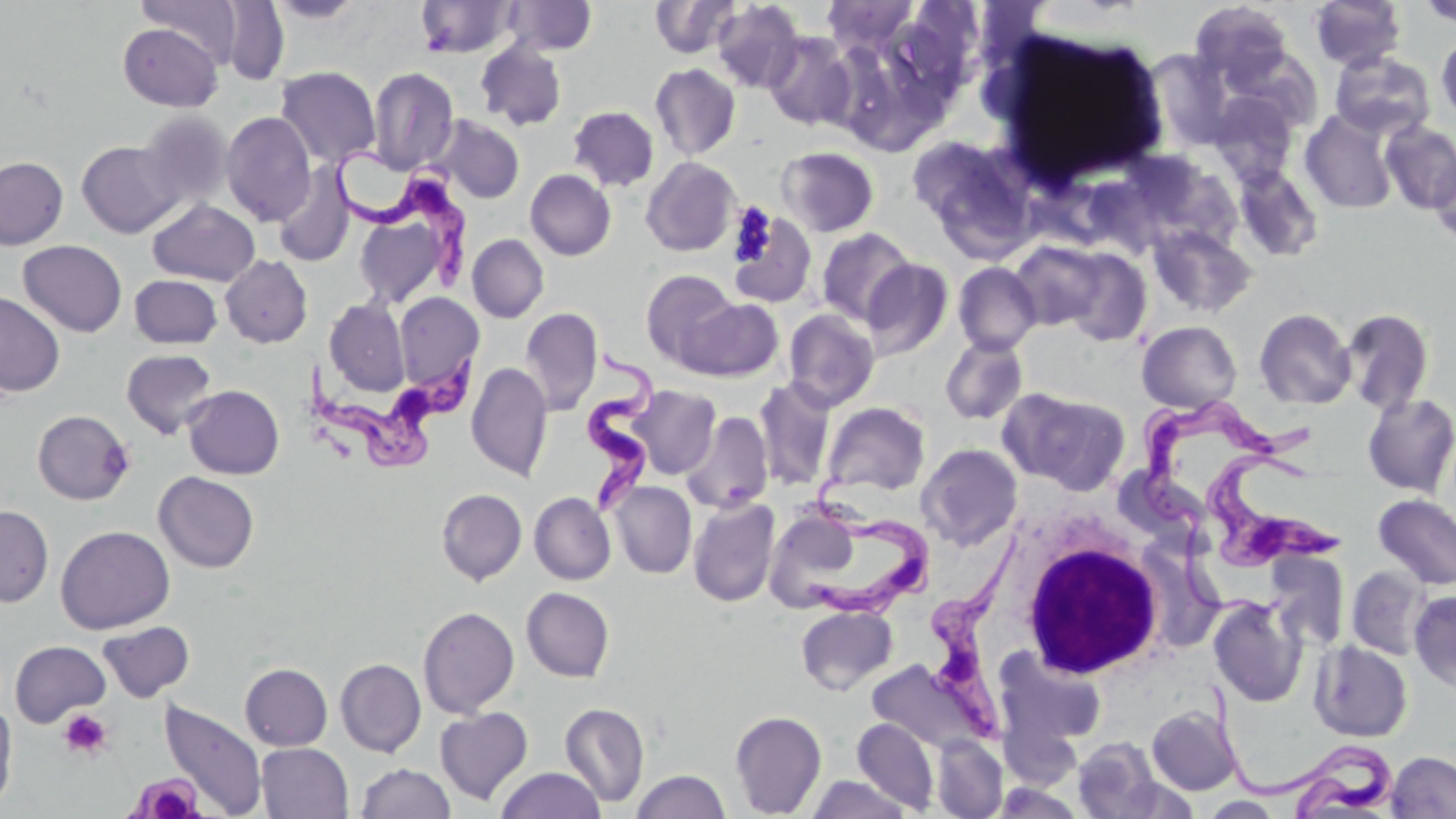
Approximate bounding boxes as [x1, y1, x2, y2] in pixels. Trypanosoma brucei locations: [335, 151, 473, 290], [576, 340, 658, 521], [303, 357, 480, 470], [1136, 397, 1325, 536], [1205, 447, 1349, 573], [800, 472, 938, 623], [924, 523, 1031, 742], [1205, 679, 1405, 819]. Uninfected red blood cell locations: [138, 0, 243, 66], [268, 0, 367, 25], [415, 0, 518, 58], [502, 0, 598, 55], [650, 0, 741, 59], [821, 0, 919, 54], [1309, 0, 1407, 72], [219, 1, 290, 84], [711, 1, 806, 93], [1416, 1, 1456, 29], [1190, 3, 1294, 88], [117, 23, 223, 112], [763, 32, 857, 131], [1435, 32, 1456, 123], [475, 42, 567, 130], [1329, 51, 1436, 140], [650, 63, 741, 161], [274, 67, 380, 169], [367, 67, 459, 176], [1209, 92, 1299, 185], [568, 106, 659, 192], [1299, 108, 1399, 215], [137, 110, 233, 211], [221, 112, 316, 226], [432, 115, 525, 204], [1380, 121, 1456, 214], [906, 134, 1039, 258], [77, 141, 181, 238], [776, 147, 879, 237], [1430, 151, 1456, 246], [0, 156, 68, 250], [641, 156, 741, 256], [273, 164, 356, 269], [1232, 164, 1324, 263], [525, 169, 616, 261], [351, 191, 464, 310], [147, 199, 260, 286], [728, 208, 818, 309], [1147, 223, 1257, 318], [815, 228, 916, 326], [467, 234, 549, 323], [1008, 239, 1116, 332], [18, 240, 126, 337], [1055, 246, 1153, 346], [220, 255, 312, 348], [860, 259, 954, 361], [952, 261, 1042, 356], [640, 269, 741, 369], [129, 275, 222, 349], [0, 291, 65, 397], [394, 292, 483, 394], [681, 297, 783, 381], [324, 298, 410, 397], [520, 307, 602, 415], [782, 308, 880, 412], [1254, 308, 1356, 410], [1340, 308, 1434, 415], [1137, 321, 1241, 413], [940, 336, 1029, 425], [121, 349, 218, 439], [466, 361, 553, 482], [753, 377, 836, 491], [183, 385, 284, 479], [626, 386, 721, 479], [1015, 390, 1131, 494], [1361, 393, 1456, 498], [821, 401, 930, 497], [33, 410, 135, 505], [680, 411, 774, 514], [918, 443, 1023, 550], [154, 471, 259, 573], [609, 481, 697, 578], [436, 488, 527, 585], [529, 492, 616, 585], [1373, 494, 1456, 591], [688, 497, 780, 607], [0, 505, 54, 606], [765, 510, 854, 613], [55, 525, 175, 633], [1346, 565, 1432, 660], [521, 587, 614, 683], [1409, 590, 1456, 691], [1208, 596, 1307, 707], [795, 605, 898, 695], [417, 606, 519, 718], [97, 621, 196, 702], [9, 640, 111, 727], [1310, 640, 1413, 742], [995, 648, 1109, 752], [335, 658, 426, 757], [240, 663, 333, 750], [0, 699, 17, 812], [157, 699, 268, 818], [560, 702, 649, 807], [1146, 705, 1242, 795], [434, 707, 533, 805], [729, 709, 826, 816], [853, 718, 939, 814], [932, 736, 1006, 818], [1072, 737, 1163, 818], [256, 743, 353, 819], [1386, 750, 1456, 818], [356, 763, 456, 819], [496, 767, 605, 819], [630, 769, 731, 819], [806, 775, 912, 819], [1202, 796, 1283, 817]. White blood cell locations: [1018, 530, 1166, 680]. Platelet locations: [729, 201, 778, 266], [58, 709, 112, 760], [127, 772, 205, 817]. Slide-level diagnosis: Trypanosoma brucei. 1000x magnification. One field of a larger specimen. Light microscopy. Image is 1456×819 pixels. Thin blood smear. May-Grünwald-Giemsa-stained preparation.